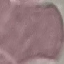
Malaria status: uninfected. Automatically extracted cell patch, resized to 64 × 64 pixels. Giemsa stain. Photographed with a smartphone camera at the microscope eyepiece. Thin smear of blood.